Classify this cell by malaria status.
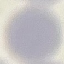
It is uninfected.

Summary:
  - Capture: smartphone camera at the microscope eyepiece
  - Preparation: thin blood smear
  - Image type: automatically extracted cell patch, resized to 64 × 64 pixels
  - Stain: Giemsa